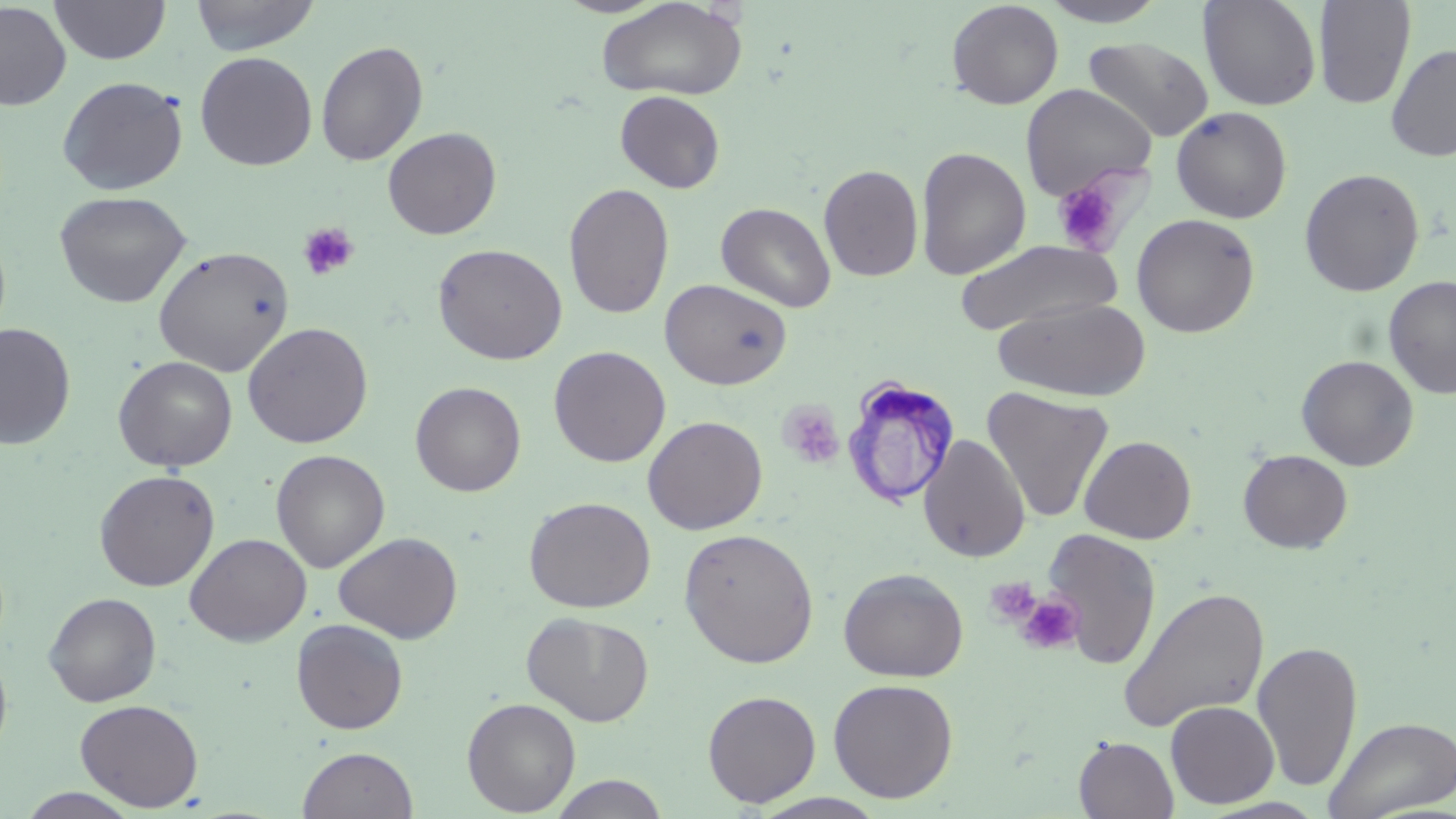

{
  "slide_level_diagnosis": "Trypanosoma brucei",
  "image_size": "1456×819 pixels",
  "field_of_view": "single",
  "preparation": "thin blood film",
  "platelet_locations": "approximate bounding boxes as (x1,y1)-(x2,y2) corner pairs in pixels: (1052,176)-(1126,256), (297,222)-(360,281), (778,402)-(845,468), (983,576)-(1041,626), (1016,595)-(1084,655)",
  "magnification": "1000x",
  "uninfected_red_blood_cell_locations": "approximate bounding boxes as (x1,y1)-(x2,y2) corner pairs in pixels: (49,0)-(171,65), (189,0)-(321,55), (595,0)-(749,101), (1038,0)-(1172,27), (1199,0)-(1321,111), (946,1)-(1064,109), (1313,1)-(1416,109), (0,2)-(72,111), (1083,36)-(1214,142), (315,40)-(428,166), (1385,43)-(1456,161), (195,51)-(317,171), (56,76)-(188,196), (1021,84)-(1156,200), (615,90)-(726,193), (1171,106)-(1292,223), (382,127)-(501,239), (915,146)-(1031,280), (818,163)-(924,282), (1299,168)-(1425,297), (563,182)-(674,320), (53,190)-(192,308), (716,202)-(836,312), (1131,213)-(1260,338), (957,239)-(1120,336), (433,243)-(568,365), (153,245)-(294,377), (1383,276)-(1456,398), (660,278)-(792,390), (993,296)-(1151,402), (243,322)-(374,448), (0,323)-(76,450), (548,346)-(671,467), (113,355)-(238,472), (1296,355)-(1419,471), (410,381)-(526,496), (981,386)-(1115,523), (642,415)-(768,534), (918,434)-(1030,562), (1079,435)-(1196,544), (271,449)-(390,573), (1238,449)-(1353,552), (94,469)-(220,591), (524,496)-(655,613), (1041,527)-(1161,671), (678,528)-(819,668), (333,531)-(463,643), (185,533)-(311,646), (839,567)-(968,682), (1117,586)-(1270,734), (44,591)-(162,706), (522,612)-(654,726), (291,618)-(408,734), (1251,640)-(1363,792), (0,646)-(13,763), (828,678)-(958,803), (702,689)-(821,807), (462,697)-(581,816), (75,698)-(204,811), (1165,700)-(1279,809), (1323,715)-(1456,818), (1073,736)-(1179,819), (297,746)-(419,819), (547,774)-(672,818), (16,788)-(144,818), (749,793)-(891,819), (1199,796)-(1330,818)",
  "trypanosoma_brucei_locations": "approximate bounding boxes as (x1,y1)-(x2,y2) corner pairs in pixels: (844,373)-(960,508)",
  "stain": "May-Grünwald-Giemsa",
  "modality": "light microscopy"
}